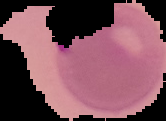

{
  "image_type": "segmented cell region on a black background",
  "preparation": "thin blood film",
  "result": "Plasmodium parasites identified",
  "image_size": "166×121 pixels"
}